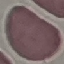

Result: negative for malaria parasites. Thin smear of blood. Automatically extracted cell patch, resized to 64 × 64 pixels. Giemsa stain. Acquired by smartphone through the microscope eyepiece.